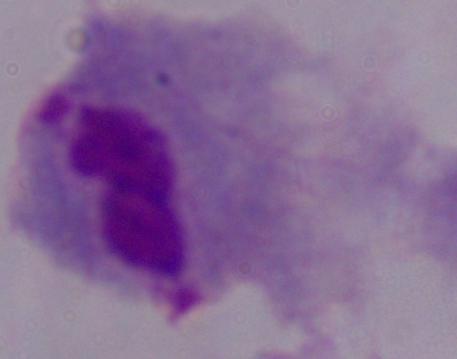
Summary:
  - Modality: micrograph
  - Identification: trichomonad
  - Magnification: 1000x